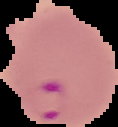
Summary:
  - Preparation: thin blood film
  - Image size: 118×127 pixels
  - Image type: segmented cell region on a black background
  - Malaria status: parasitized